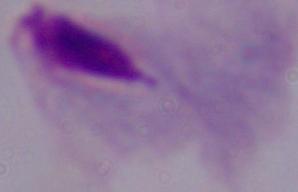
Photomicrograph. A trichomonad is shown. Captured at 1000x magnification.